Assess this cell for malaria.
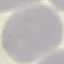

Uninfected.

stain: Giemsa
capture: smartphone through the microscope eyepiece
preparation: thin blood smear
image_type: cell patch, automatically extracted from a larger field of view and resized to 64 × 64 pixels